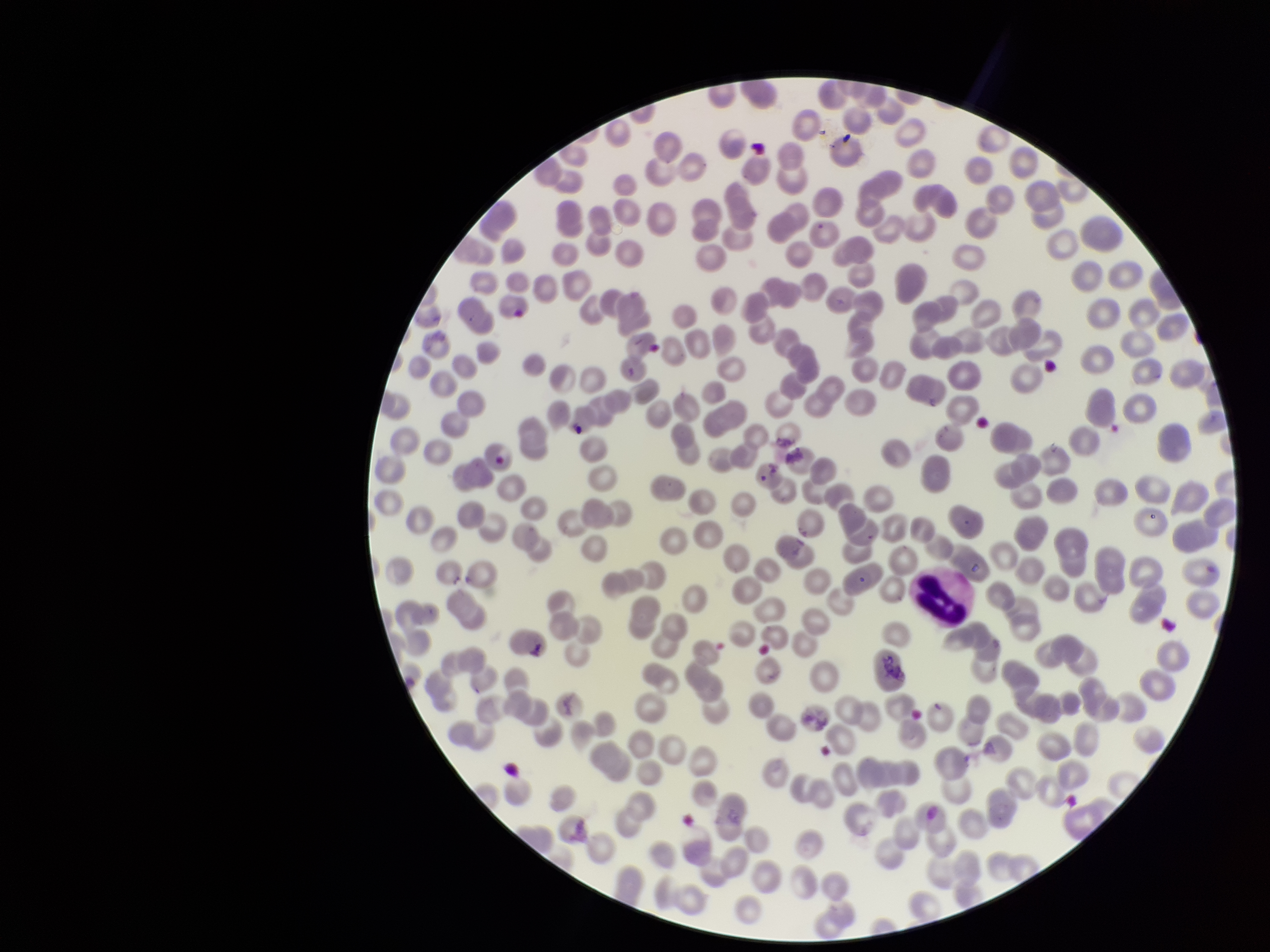

Summary:
  - Red blood cell count: 269
  - Capture: smartphone photograph through the microscope eyepiece
  - Image size: 1270×952 pixels
  - Parasitized red blood cells: none detected
  - Stain: Giemsa
  - Parasitized red blood cell count: 0
  - Preparation: thin blood smear
  - Patient malaria status: negative
  - Field of view: single